Give the position of every malaria parasite.
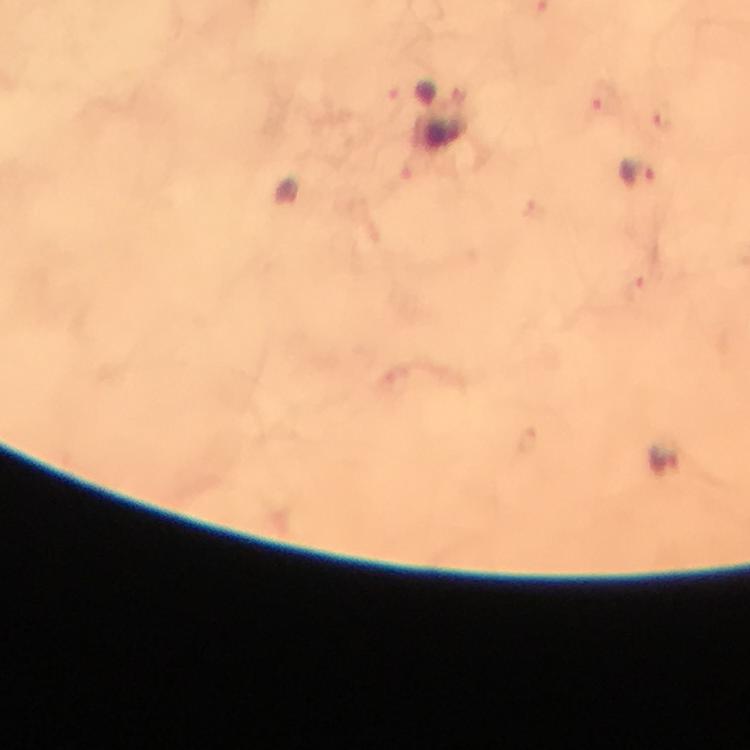

Approximate object centers, in pixels from the top-left corner.
Malaria parasites: (x=443, y=135), (x=642, y=174), (x=666, y=460).

Summary:
  - Stain: Giemsa
  - Context: from a diagnostic examination for malaria
  - Cropped from: one field of view
  - Magnification: 100x
  - Capture: smartphone mounted on the microscope
  - Image size: 750×750 pixels
  - Preparation: thick blood smear
  - Immersion oil: applied